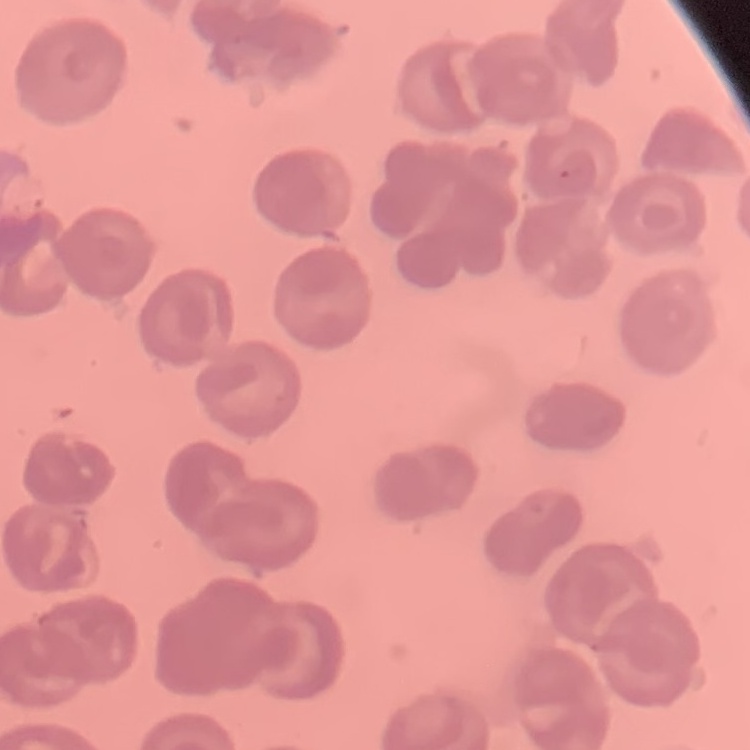
red_blood_cell_morphology: no rouleaux formation
stain: Field's or Giemsa
image_type: square crop of a larger photomicrograph
preparation: thin blood film